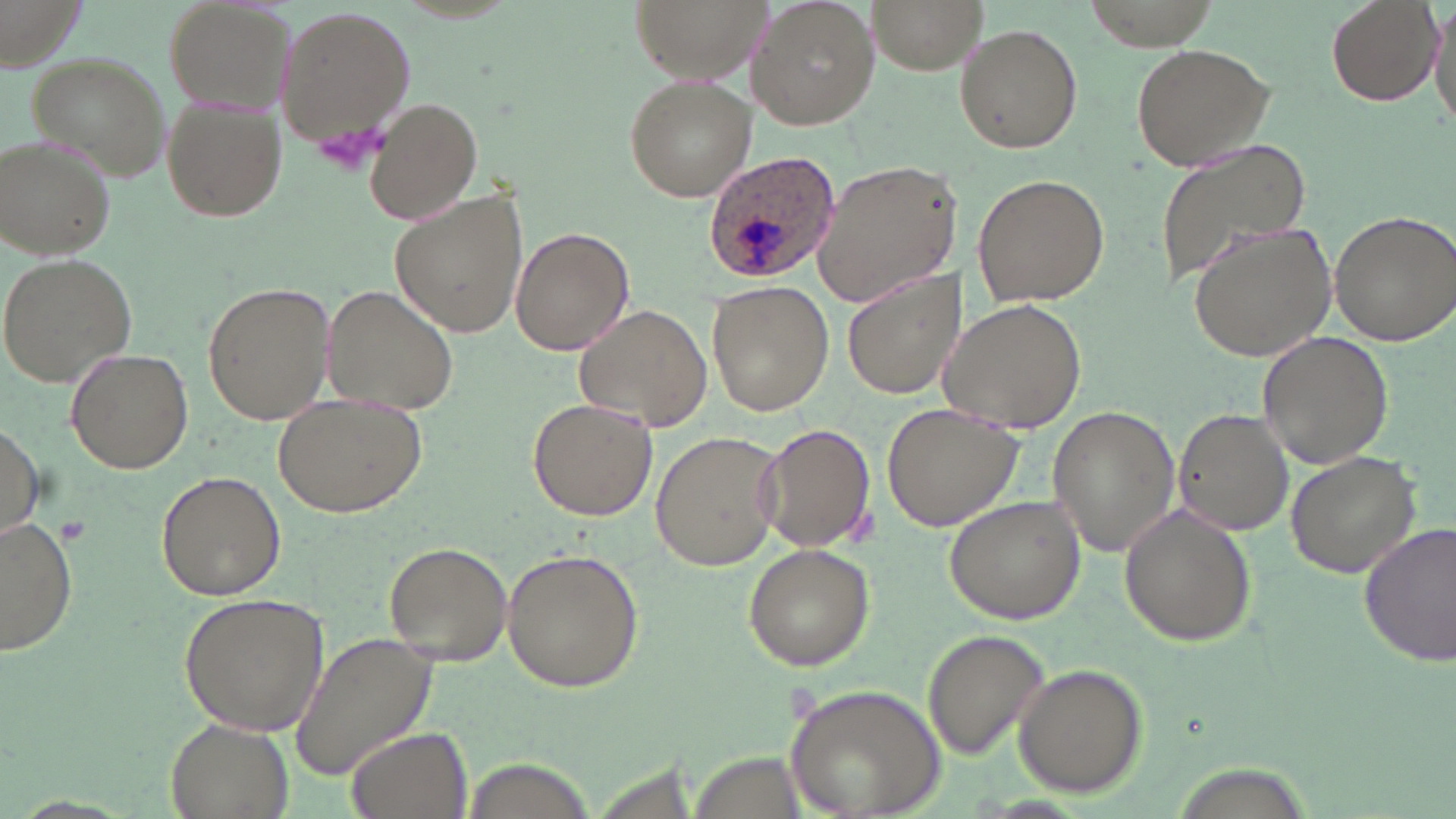

Summary:
  - Coordinate format: approximate bounding boxes as [x1, y1, x2, y2] in pixels
  - Uninfected red blood cell locations: [162, 0, 300, 113], [630, 0, 770, 84], [745, 0, 879, 130], [867, 0, 985, 74], [1324, 0, 1443, 106], [1429, 0, 1456, 141], [275, 4, 415, 147], [954, 24, 1082, 153], [1130, 42, 1276, 173], [27, 53, 169, 182], [623, 75, 756, 202], [161, 96, 287, 223], [365, 97, 484, 224], [1, 136, 117, 260], [1153, 138, 1314, 288], [810, 160, 962, 307], [973, 172, 1111, 308], [390, 190, 529, 341], [1329, 209, 1456, 345], [1187, 221, 1340, 361], [511, 226, 632, 355], [0, 251, 136, 389], [842, 270, 963, 399], [201, 279, 336, 427], [706, 282, 835, 416], [324, 285, 457, 416], [940, 297, 1088, 437], [576, 304, 712, 431], [1255, 330, 1393, 470], [65, 347, 193, 474], [271, 396, 426, 518], [526, 397, 657, 521], [882, 402, 1026, 533], [1048, 404, 1181, 558], [1172, 408, 1294, 537], [0, 420, 45, 540], [759, 423, 877, 553], [650, 429, 782, 571], [1283, 450, 1423, 580], [155, 467, 287, 601], [943, 495, 1086, 625], [1119, 503, 1257, 647], [3, 520, 79, 655], [1357, 522, 1456, 668], [742, 542, 877, 671], [382, 543, 511, 664], [502, 547, 646, 694], [177, 592, 330, 736], [921, 628, 1051, 763], [289, 630, 438, 781], [1014, 664, 1147, 796], [784, 684, 946, 819], [168, 719, 294, 818], [343, 727, 473, 819], [465, 757, 594, 818]
  - Platelet locations: [313, 119, 383, 177], [56, 516, 93, 546]
  - Plasmodium ovale-infected red blood cell locations: [700, 148, 844, 286]
  - Slide-level diagnosis: Plasmodium ovale
  - Modality: light microscopy
  - Field of view: single
  - Preparation: thin blood smear
  - Image size: 1456×819 pixels
  - Magnification: 1000x
  - Stain: May-Grünwald-Giemsa